Assess the morphology of the red blood cells.
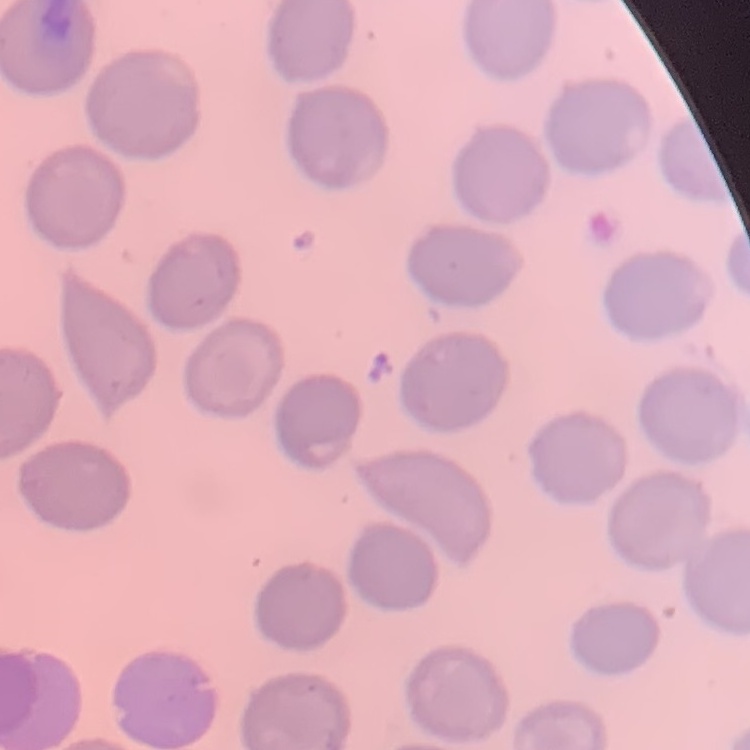
They show no rouleaux formation.

image type = square crop of a larger photomicrograph
stain = Field's or Giemsa
preparation = thin peripheral smear